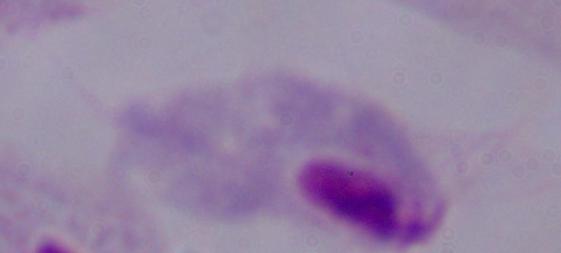

Photomicrograph. A trichomonad is seen. 1000x magnification.